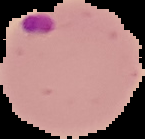
Summary:
  - Malaria status: parasitized
  - Preparation: thin blood film
  - Image size: 145×139 pixels
  - Image type: segmented cell region with the area outside set to black